Classify this cell by malaria status.
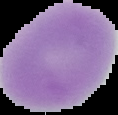
It is uninfected.

The area outside the segmented cell region is set to black. From a thin blood smear. Image is 118×115 pixels.